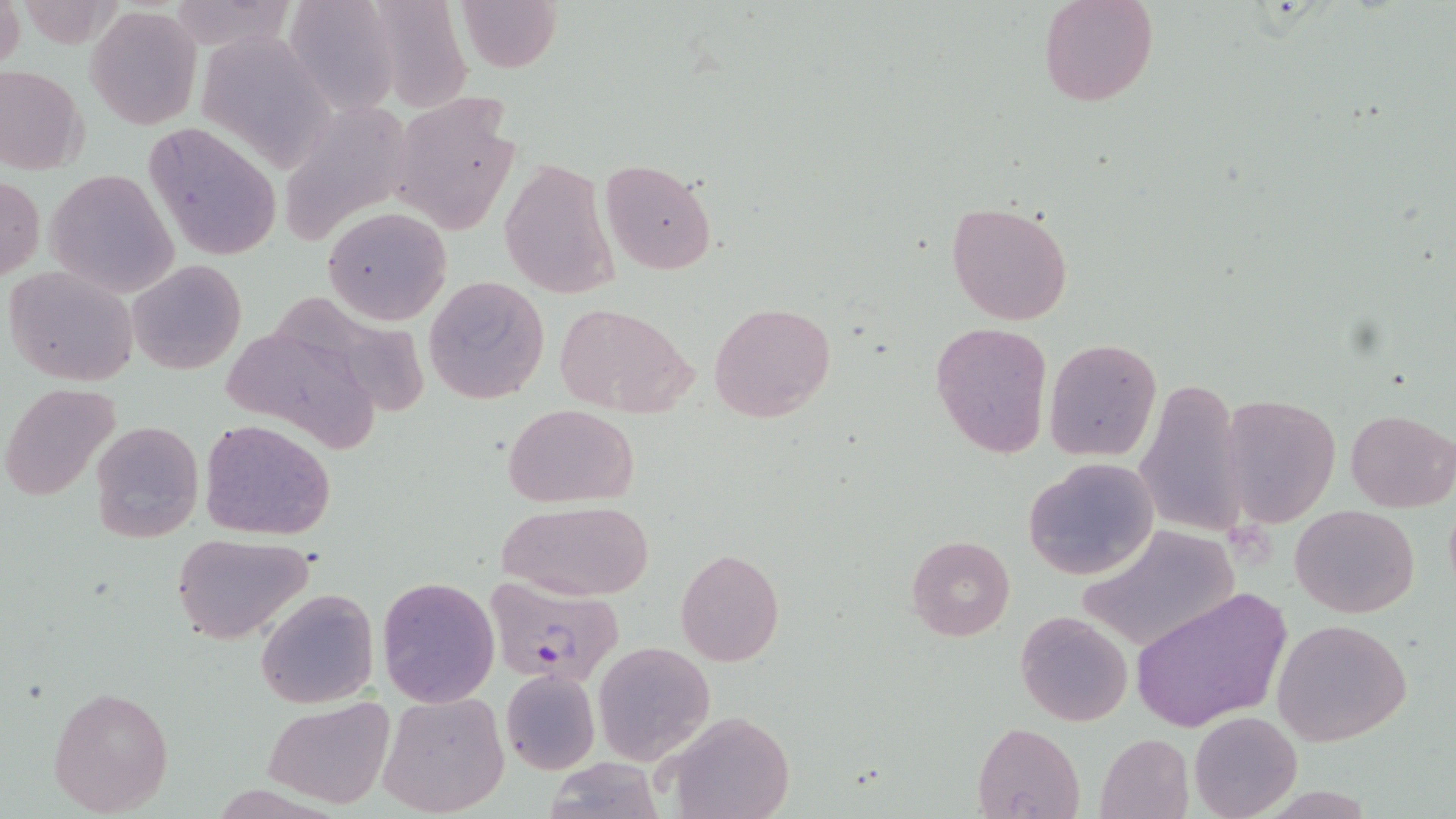 Approximate bounding boxes as named x1/y1/x2/y2 corners in pixels. Uninfected red blood cell locations: (x1=0, y1=0, x2=23, y2=74), (x1=164, y1=0, x2=298, y2=53), (x1=454, y1=0, x2=563, y2=72), (x1=1039, y1=0, x2=1159, y2=107), (x1=374, y1=1, x2=476, y2=115), (x1=288, y1=2, x2=409, y2=122), (x1=85, y1=4, x2=202, y2=130), (x1=194, y1=28, x2=334, y2=177), (x1=0, y1=64, x2=89, y2=176), (x1=392, y1=92, x2=522, y2=237), (x1=283, y1=99, x2=413, y2=247), (x1=141, y1=121, x2=284, y2=263), (x1=500, y1=156, x2=618, y2=300), (x1=600, y1=159, x2=718, y2=276), (x1=47, y1=169, x2=179, y2=298), (x1=0, y1=175, x2=45, y2=284), (x1=945, y1=201, x2=1075, y2=326), (x1=323, y1=207, x2=451, y2=325), (x1=128, y1=258, x2=246, y2=374), (x1=4, y1=263, x2=140, y2=386), (x1=424, y1=275, x2=550, y2=404), (x1=283, y1=296, x2=432, y2=416), (x1=708, y1=301, x2=836, y2=421), (x1=558, y1=303, x2=696, y2=416), (x1=930, y1=320, x2=1052, y2=459), (x1=212, y1=332, x2=365, y2=441), (x1=1044, y1=337, x2=1162, y2=460), (x1=1134, y1=379, x2=1248, y2=538), (x1=2, y1=382, x2=123, y2=504), (x1=1222, y1=391, x2=1340, y2=528), (x1=503, y1=403, x2=640, y2=507), (x1=1345, y1=407, x2=1456, y2=513), (x1=198, y1=417, x2=336, y2=539), (x1=89, y1=418, x2=205, y2=544), (x1=1023, y1=457, x2=1157, y2=580), (x1=494, y1=499, x2=655, y2=602), (x1=1291, y1=503, x2=1420, y2=618), (x1=1076, y1=523, x2=1239, y2=653), (x1=171, y1=533, x2=315, y2=645), (x1=905, y1=535, x2=1015, y2=640), (x1=675, y1=547, x2=785, y2=666), (x1=377, y1=575, x2=500, y2=707), (x1=1130, y1=586, x2=1291, y2=732), (x1=256, y1=588, x2=379, y2=710), (x1=1016, y1=611, x2=1134, y2=726), (x1=1270, y1=619, x2=1413, y2=745), (x1=593, y1=640, x2=715, y2=766), (x1=499, y1=669, x2=599, y2=775), (x1=48, y1=683, x2=173, y2=816), (x1=377, y1=690, x2=510, y2=816), (x1=262, y1=698, x2=395, y2=811), (x1=1189, y1=710, x2=1302, y2=819), (x1=663, y1=711, x2=796, y2=819), (x1=973, y1=721, x2=1087, y2=818), (x1=1095, y1=732, x2=1195, y2=818). Plasmodium falciparum-infected red blood cell locations: (x1=485, y1=579, x2=625, y2=689). Slide-level diagnosis: Plasmodium falciparum. Image is 1456×819 pixels. One field of a larger specimen. Optical microscopy. 1000x magnification. Thin blood smear. May-Grünwald-Giemsa stain.